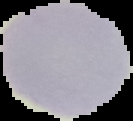
Image is 133×121 pixels. Segmented cell region on a black background. From a thin blood film. Result: no Plasmodium parasites detected.